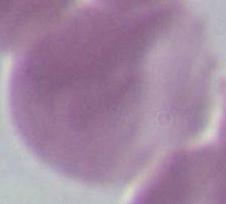

modality = photomicrograph
magnification = 1000x
identification = erythrocyte